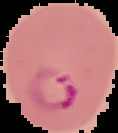
Summary:
  - Result: Plasmodium parasites detected
  - Preparation: thin blood film
  - Image size: 118×133 pixels
  - Image type: segmented cell region on a black background